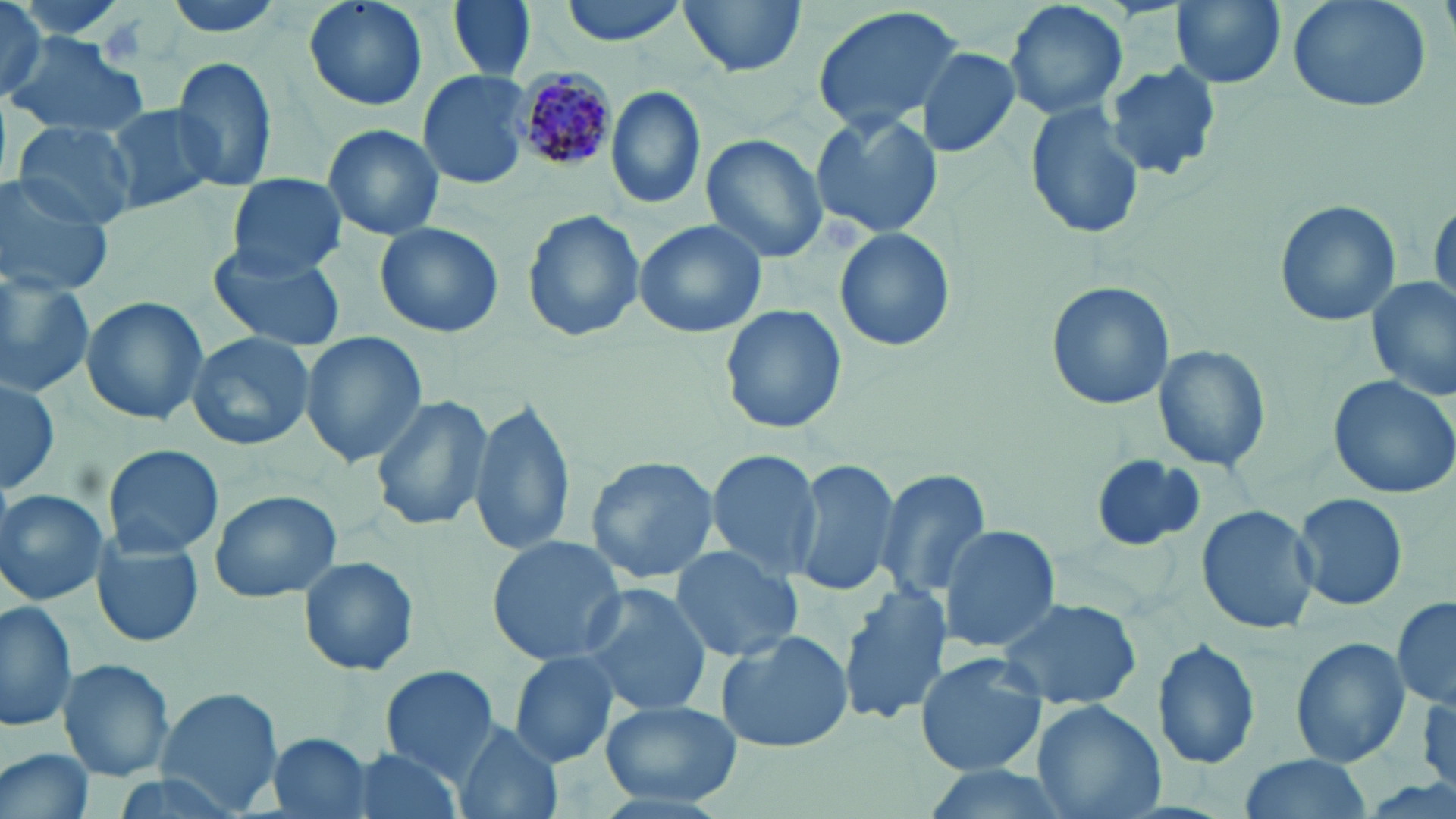
slide-level diagnosis = Plasmodium malariae
magnification = 1000x
uninfected red blood cell locations = approximate bounding boxes as named x1/y1/x2/y2 corners in pixels: (x1=157, y1=0, x2=293, y2=41), (x1=301, y1=0, x2=429, y2=114), (x1=449, y1=0, x2=536, y2=82), (x1=556, y1=0, x2=695, y2=46), (x1=679, y1=0, x2=804, y2=79), (x1=1004, y1=0, x2=1127, y2=122), (x1=1171, y1=0, x2=1285, y2=90), (x1=1281, y1=0, x2=1435, y2=114), (x1=806, y1=6, x2=967, y2=135), (x1=0, y1=7, x2=82, y2=109), (x1=5, y1=35, x2=147, y2=138), (x1=915, y1=46, x2=1022, y2=158), (x1=169, y1=54, x2=279, y2=191), (x1=1103, y1=61, x2=1226, y2=181), (x1=416, y1=69, x2=534, y2=191), (x1=606, y1=85, x2=707, y2=212), (x1=1024, y1=101, x2=1146, y2=240), (x1=106, y1=103, x2=222, y2=215), (x1=810, y1=111, x2=945, y2=241), (x1=13, y1=120, x2=139, y2=230), (x1=322, y1=123, x2=444, y2=242), (x1=700, y1=133, x2=828, y2=264), (x1=226, y1=172, x2=347, y2=278), (x1=0, y1=175, x2=115, y2=297), (x1=1428, y1=194, x2=1455, y2=317), (x1=1274, y1=200, x2=1401, y2=326), (x1=521, y1=207, x2=646, y2=343), (x1=633, y1=219, x2=768, y2=340), (x1=373, y1=221, x2=505, y2=339), (x1=835, y1=227, x2=957, y2=353), (x1=209, y1=247, x2=346, y2=351), (x1=0, y1=273, x2=96, y2=395), (x1=1367, y1=278, x2=1455, y2=405), (x1=1044, y1=279, x2=1174, y2=410), (x1=80, y1=296, x2=208, y2=427), (x1=719, y1=304, x2=846, y2=435), (x1=186, y1=331, x2=317, y2=450), (x1=299, y1=332, x2=428, y2=468), (x1=1151, y1=344, x2=1271, y2=473), (x1=1326, y1=374, x2=1456, y2=500), (x1=0, y1=375, x2=62, y2=495), (x1=368, y1=393, x2=496, y2=532), (x1=471, y1=399, x2=575, y2=555), (x1=103, y1=443, x2=224, y2=559), (x1=706, y1=449, x2=823, y2=580), (x1=1090, y1=453, x2=1205, y2=551), (x1=582, y1=455, x2=721, y2=585), (x1=791, y1=457, x2=902, y2=598), (x1=874, y1=467, x2=992, y2=602), (x1=1, y1=488, x2=109, y2=607), (x1=208, y1=489, x2=342, y2=604), (x1=1292, y1=491, x2=1408, y2=611), (x1=1195, y1=504, x2=1320, y2=636), (x1=938, y1=524, x2=1060, y2=653), (x1=486, y1=535, x2=628, y2=665), (x1=93, y1=538, x2=206, y2=647), (x1=669, y1=545, x2=805, y2=663), (x1=297, y1=556, x2=421, y2=678), (x1=839, y1=583, x2=952, y2=727), (x1=575, y1=584, x2=713, y2=716), (x1=996, y1=595, x2=1144, y2=714), (x1=1392, y1=597, x2=1456, y2=711), (x1=0, y1=599, x2=79, y2=734), (x1=715, y1=628, x2=851, y2=754), (x1=1290, y1=638, x2=1412, y2=768), (x1=1152, y1=639, x2=1261, y2=770), (x1=509, y1=652, x2=621, y2=767), (x1=915, y1=652, x2=1050, y2=779), (x1=59, y1=659, x2=174, y2=785), (x1=378, y1=665, x2=501, y2=783), (x1=154, y1=687, x2=284, y2=815), (x1=602, y1=698, x2=742, y2=807), (x1=1031, y1=699, x2=1167, y2=819), (x1=455, y1=723, x2=563, y2=819), (x1=267, y1=732, x2=373, y2=817), (x1=2, y1=743, x2=96, y2=819), (x1=346, y1=746, x2=465, y2=819), (x1=1236, y1=754, x2=1373, y2=819), (x1=909, y1=763, x2=1072, y2=819)
preparation = thin blood smear
stain = May-Grünwald-Giemsa
image size = 1456×819 pixels
field of view = single
Plasmodium malariae-infected red blood cell locations = approximate bounding boxes as named x1/y1/x2/y2 corners in pixels: (x1=515, y1=71, x2=618, y2=173)
modality = light microscopy